Locate every malaria parasite.
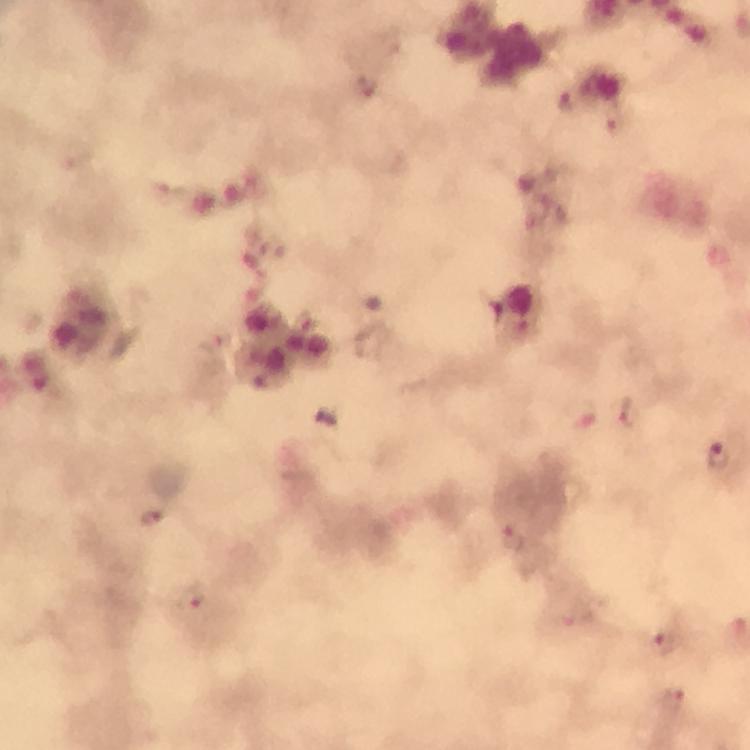
Approximate object centers, in pixels from the top-left corner.
Malaria parasites: (x=367, y=87), (x=616, y=120), (x=629, y=412), (x=719, y=455), (x=512, y=537), (x=577, y=616), (x=665, y=645), (x=671, y=700).

A crop from one field of view. Immersion oil applied. From a diagnostic examination for malaria. Thick smear. Photographed through the microscope with a smartphone camera. Image is 750×750 pixels. 100x magnification. Giemsa-stained preparation.